Report the malaria status of this cell.
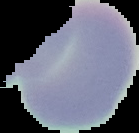
It is uninfected.

preparation = thin blood film
image type = segmented cell region with the area outside set to black
image size = 139×133 pixels